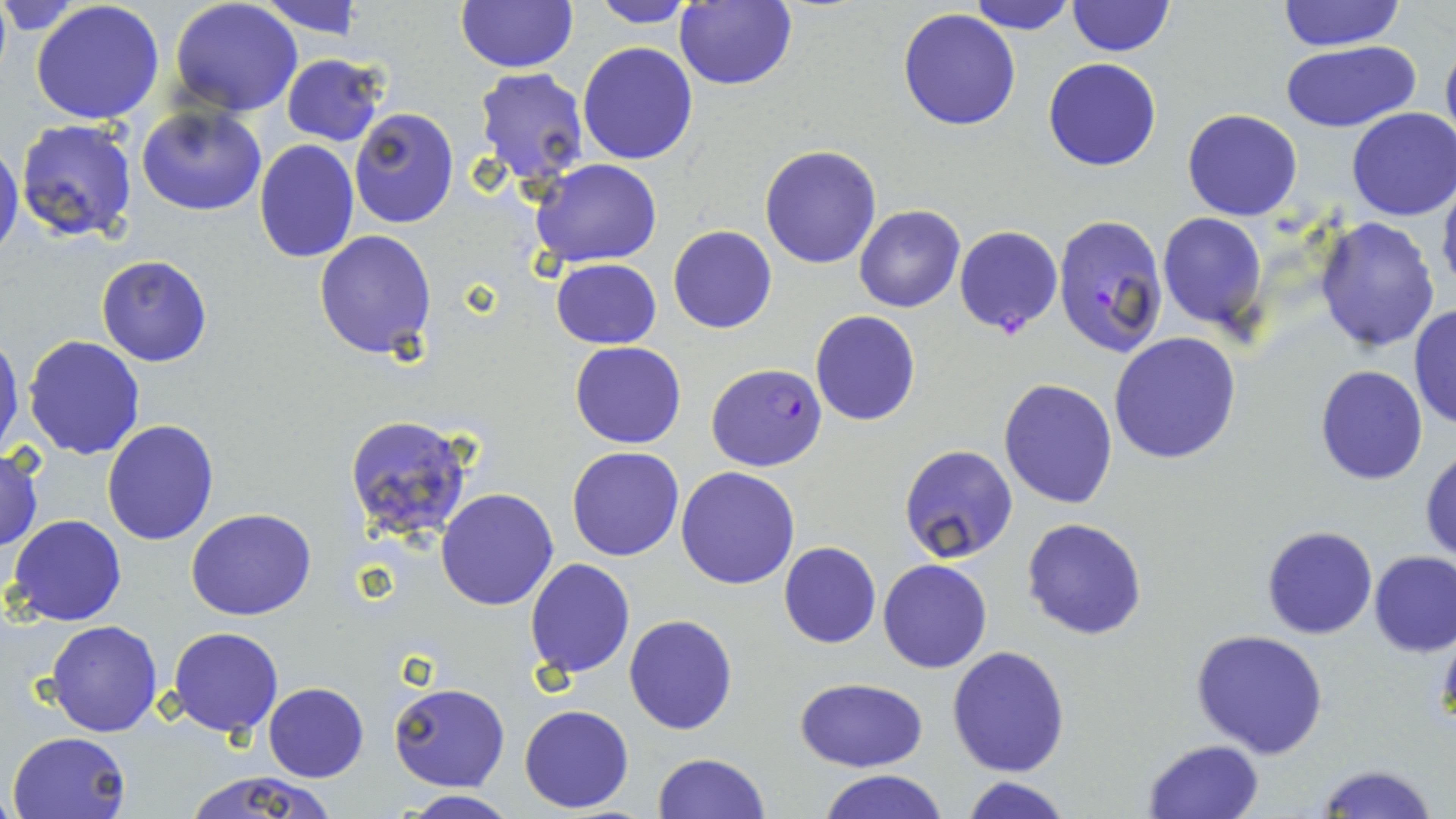

Approximate bounding boxes as [x1, y1, x2, y2] in pixels. Uninfected red blood cell locations: [32, 0, 165, 124], [171, 0, 303, 116], [676, 0, 798, 91], [1276, 0, 1405, 51], [257, 1, 366, 38], [457, 1, 577, 73], [588, 1, 701, 27], [967, 1, 1077, 35], [1066, 1, 1176, 57], [898, 9, 1021, 131], [1440, 34, 1456, 160], [1280, 39, 1422, 132], [577, 41, 700, 165], [282, 52, 386, 146], [1043, 58, 1162, 171], [473, 68, 590, 185], [137, 104, 266, 215], [348, 106, 459, 229], [1182, 108, 1303, 221], [1346, 109, 1455, 222], [16, 118, 141, 245], [253, 139, 359, 262], [0, 141, 24, 263], [760, 144, 882, 269], [531, 159, 663, 269], [1437, 178, 1456, 300], [854, 205, 965, 313], [1156, 211, 1268, 331], [1313, 217, 1441, 356], [668, 225, 778, 334], [313, 229, 436, 359], [96, 254, 213, 367], [559, 254, 671, 445], [551, 258, 661, 348], [1411, 303, 1455, 433], [811, 312, 921, 427], [1108, 331, 1243, 464], [0, 332, 24, 457], [23, 335, 146, 459], [570, 342, 686, 448], [1315, 365, 1428, 485], [998, 378, 1117, 509], [342, 414, 478, 545], [100, 420, 220, 544], [0, 445, 43, 554], [899, 445, 1018, 564], [1420, 445, 1455, 562], [567, 447, 684, 561], [676, 466, 799, 589], [436, 488, 559, 610], [186, 508, 316, 621], [7, 514, 127, 626], [1022, 517, 1148, 639], [1262, 525, 1377, 639], [779, 541, 881, 649], [1368, 550, 1456, 657], [524, 557, 635, 679], [878, 559, 992, 672], [623, 613, 738, 735], [47, 619, 163, 737], [168, 626, 282, 737], [1191, 628, 1331, 758], [947, 645, 1070, 777], [792, 677, 928, 772], [262, 682, 368, 782], [389, 683, 509, 790], [519, 705, 634, 812], [8, 732, 131, 819], [1142, 738, 1266, 819], [652, 752, 769, 819], [1313, 763, 1438, 819], [180, 769, 337, 819], [817, 770, 948, 819], [958, 776, 1074, 819], [397, 792, 518, 819]. Plasmodium falciparum-infected red blood cell locations: [1052, 215, 1168, 363], [953, 226, 1064, 335], [705, 363, 827, 471]. Slide-level diagnosis: Plasmodium falciparum. Thin blood film. Single field of view. Image is 1456×819 pixels. May-Grünwald-Giemsa stain. Optical microscopy. 1000x magnification.